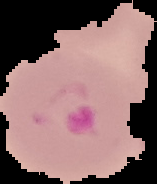

Summary:
  - Preparation: thin blood smear
  - Result: no malaria parasites seen
  - Image size: 157×184 pixels
  - Image type: segmented cell region on a black background